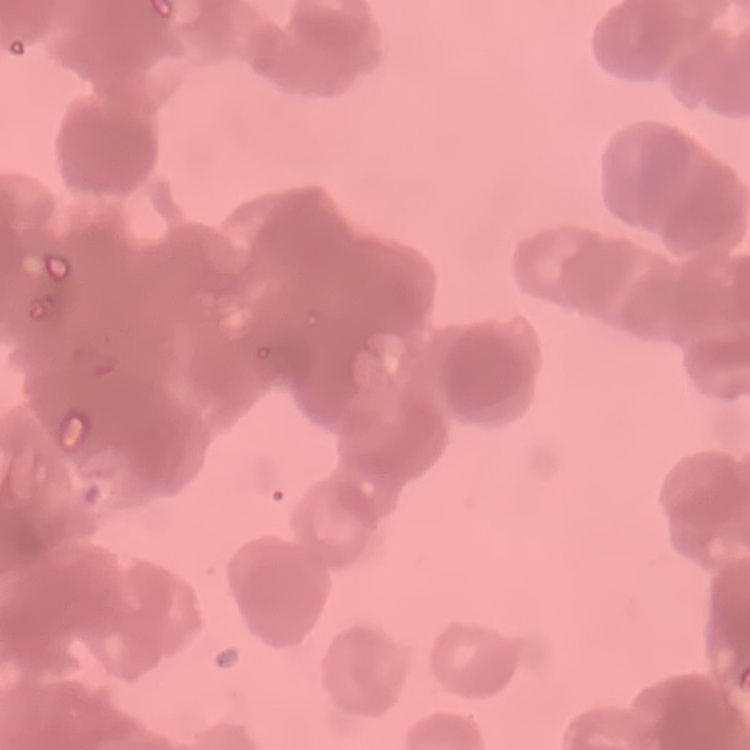
{
  "erythrocyte_morphology": "rouleaux formation",
  "stain": "Field's or Giemsa",
  "preparation": "thin blood smear",
  "image_type": "one tile cut from a larger photomicrograph"
}